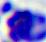 Micrograph. 400x magnification. A white blood cell is shown.